Name the blood parasite species.
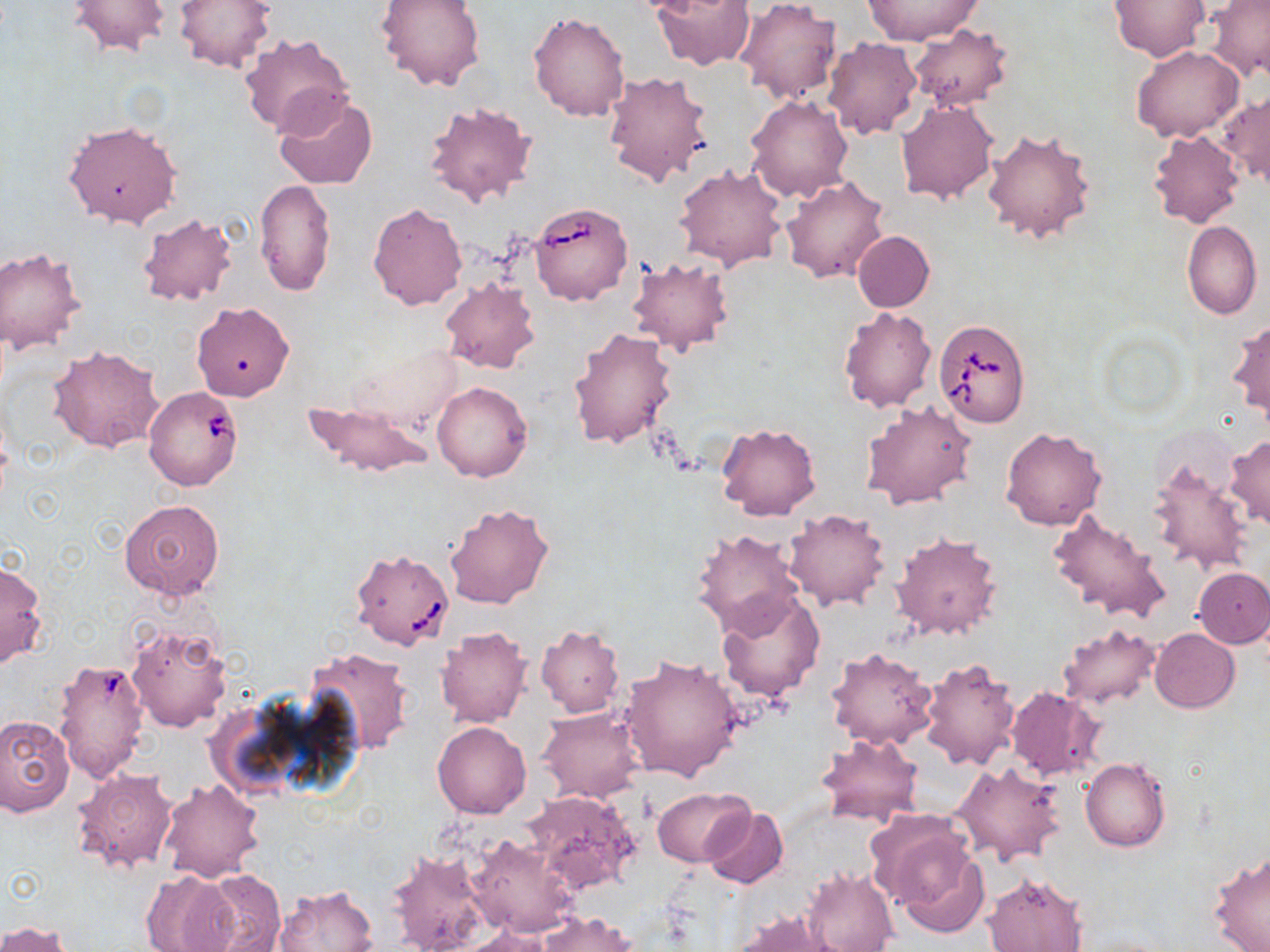

Babesia divergens.

Approximate bounding boxes as (x1, y1, x2, y2) in pixels. Babesia divergens-infected red blood cell locations: (529, 201, 632, 305), (933, 319, 1030, 427), (144, 386, 243, 491), (350, 548, 455, 650), (53, 658, 151, 782). Uninfected red blood cell locations: (176, 0, 275, 72), (375, 0, 485, 91), (652, 0, 756, 71), (863, 0, 983, 45), (1108, 0, 1210, 62), (1207, 0, 1270, 82), (68, 1, 170, 57), (736, 1, 841, 103), (528, 12, 631, 121), (909, 24, 1013, 111), (240, 34, 353, 138), (822, 38, 921, 140), (1132, 46, 1243, 141), (602, 71, 713, 189), (273, 92, 378, 189), (1221, 92, 1270, 187), (746, 94, 853, 203), (896, 100, 997, 204), (422, 101, 538, 209), (62, 120, 182, 229), (982, 127, 1097, 244), (1148, 130, 1244, 228), (674, 165, 790, 271), (781, 175, 889, 284), (253, 178, 335, 298), (368, 203, 467, 311), (137, 212, 238, 307), (1181, 220, 1262, 320), (852, 230, 934, 312), (0, 247, 86, 355), (627, 256, 734, 356), (439, 278, 540, 374), (192, 301, 294, 401), (838, 306, 936, 412), (1228, 318, 1270, 425), (569, 327, 677, 449), (48, 345, 164, 454), (347, 345, 462, 431), (432, 382, 532, 481), (303, 400, 434, 479), (862, 400, 975, 510), (715, 423, 822, 520), (1001, 428, 1106, 531), (1225, 435, 1270, 529), (1147, 457, 1252, 574), (119, 498, 224, 602), (444, 502, 555, 609), (781, 509, 889, 612), (1048, 509, 1170, 627), (692, 528, 804, 634), (890, 530, 1003, 641), (0, 560, 48, 668), (1193, 569, 1270, 647), (716, 589, 826, 704), (125, 622, 232, 731), (1058, 624, 1162, 709), (435, 625, 531, 728), (534, 626, 625, 717), (1150, 628, 1240, 712), (306, 647, 415, 756), (825, 647, 938, 751), (619, 654, 746, 782), (918, 658, 1020, 771), (1006, 687, 1106, 782), (538, 708, 644, 803), (0, 715, 74, 815), (432, 721, 530, 819), (815, 734, 922, 827), (1081, 757, 1171, 852), (950, 761, 1067, 864), (70, 766, 178, 875), (158, 779, 266, 883), (651, 786, 751, 867), (524, 791, 639, 892), (701, 808, 788, 889), (879, 821, 991, 934), (464, 832, 581, 938), (385, 848, 491, 952), (1208, 851, 1270, 952), (801, 866, 899, 952), (139, 869, 238, 952), (190, 869, 286, 952), (983, 873, 1088, 952), (273, 886, 377, 952), (730, 909, 839, 952), (536, 911, 636, 952), (0, 920, 74, 952), (453, 927, 555, 951). May-Grünwald-Giemsa-stained preparation. Optical microscopy. Thin blood film. Image is 1270×952 pixels. 1000x magnification. One field of a larger specimen.